Outline each Plasmodium ovale-infected red blood cell.
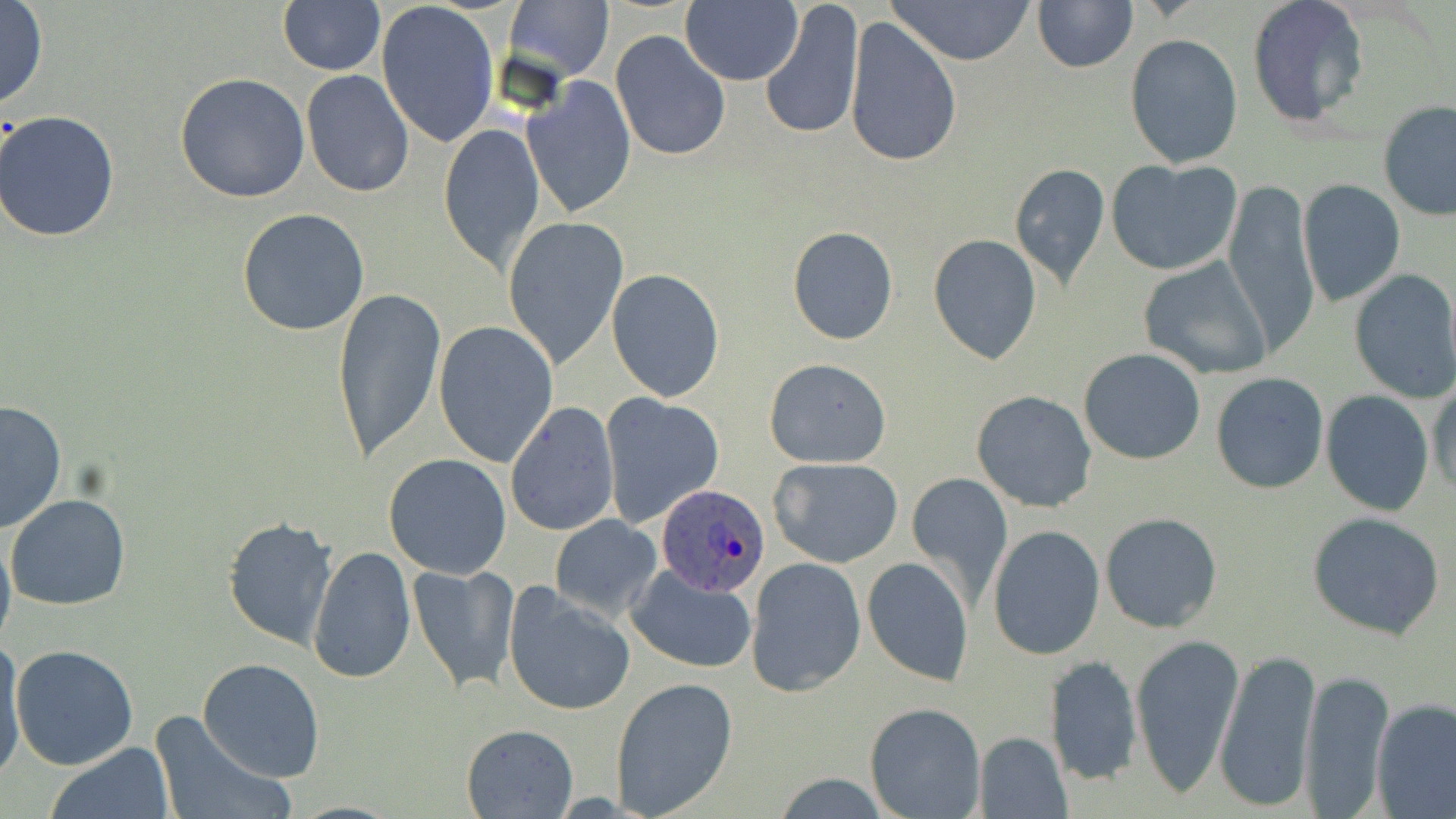
Approximate bounding boxes as named x1/y1/x2/y2 corners in pixels.
Plasmodium ovale-infected red blood cells: (x1=658, y1=485, x2=769, y2=596).

Summary:
  - Uninfected red blood cell locations: (x1=278, y1=0, x2=387, y2=76), (x1=887, y1=0, x2=1037, y2=65), (x1=1247, y1=0, x2=1369, y2=129), (x1=376, y1=1, x2=499, y2=147), (x1=504, y1=1, x2=614, y2=81), (x1=1032, y1=1, x2=1137, y2=73), (x1=0, y1=2, x2=48, y2=108), (x1=681, y1=2, x2=802, y2=85), (x1=760, y1=2, x2=865, y2=143), (x1=844, y1=17, x2=960, y2=168), (x1=611, y1=30, x2=730, y2=162), (x1=1125, y1=34, x2=1243, y2=168), (x1=301, y1=69, x2=415, y2=195), (x1=174, y1=73, x2=310, y2=205), (x1=521, y1=75, x2=635, y2=217), (x1=1378, y1=103, x2=1456, y2=221), (x1=0, y1=111, x2=122, y2=243), (x1=438, y1=122, x2=546, y2=271), (x1=1108, y1=158, x2=1242, y2=276), (x1=1009, y1=163, x2=1111, y2=288), (x1=1222, y1=180, x2=1317, y2=352), (x1=1297, y1=180, x2=1405, y2=307), (x1=237, y1=207, x2=370, y2=336), (x1=502, y1=215, x2=630, y2=371), (x1=787, y1=227, x2=898, y2=344), (x1=927, y1=233, x2=1043, y2=365), (x1=1137, y1=256, x2=1273, y2=381), (x1=605, y1=268, x2=726, y2=400), (x1=1347, y1=269, x2=1456, y2=402), (x1=330, y1=284, x2=447, y2=464), (x1=434, y1=322, x2=560, y2=467), (x1=1079, y1=348, x2=1205, y2=464), (x1=763, y1=357, x2=892, y2=467), (x1=1211, y1=371, x2=1329, y2=495), (x1=1429, y1=379, x2=1455, y2=499), (x1=972, y1=390, x2=1096, y2=513), (x1=1321, y1=391, x2=1434, y2=515), (x1=598, y1=393, x2=725, y2=526), (x1=1, y1=399, x2=67, y2=533), (x1=503, y1=401, x2=618, y2=538), (x1=383, y1=452, x2=513, y2=578), (x1=768, y1=455, x2=905, y2=569), (x1=907, y1=470, x2=1012, y2=605), (x1=5, y1=493, x2=131, y2=610), (x1=1099, y1=511, x2=1222, y2=634), (x1=1306, y1=512, x2=1445, y2=641), (x1=223, y1=514, x2=337, y2=649), (x1=549, y1=514, x2=663, y2=619), (x1=988, y1=524, x2=1105, y2=660), (x1=0, y1=527, x2=15, y2=656), (x1=306, y1=544, x2=415, y2=686), (x1=862, y1=555, x2=974, y2=688), (x1=745, y1=556, x2=865, y2=696), (x1=407, y1=562, x2=522, y2=693), (x1=626, y1=565, x2=757, y2=673), (x1=504, y1=586, x2=637, y2=716), (x1=1130, y1=633, x2=1244, y2=798), (x1=1, y1=637, x2=28, y2=784), (x1=9, y1=645, x2=138, y2=770), (x1=1213, y1=647, x2=1321, y2=813), (x1=1047, y1=652, x2=1143, y2=788), (x1=197, y1=658, x2=326, y2=784), (x1=1298, y1=669, x2=1394, y2=814), (x1=609, y1=677, x2=740, y2=818), (x1=1371, y1=698, x2=1456, y2=818), (x1=863, y1=701, x2=986, y2=818), (x1=149, y1=710, x2=291, y2=819), (x1=460, y1=723, x2=578, y2=817), (x1=973, y1=731, x2=1072, y2=818), (x1=45, y1=742, x2=174, y2=819)
  - Slide-level diagnosis: Plasmodium ovale
  - Field of view: single
  - Modality: optical microscopy
  - Image size: 1456×819 pixels
  - Preparation: thin blood film
  - Stain: May-Grünwald-Giemsa
  - Magnification: 1000x